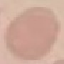

Malaria status: uninfected. Giemsa-stained preparation. Thin blood smear. Acquired by smartphone through the microscope eyepiece. Cell patch, automatically extracted from a larger field of view and resized to 64 × 64 pixels.